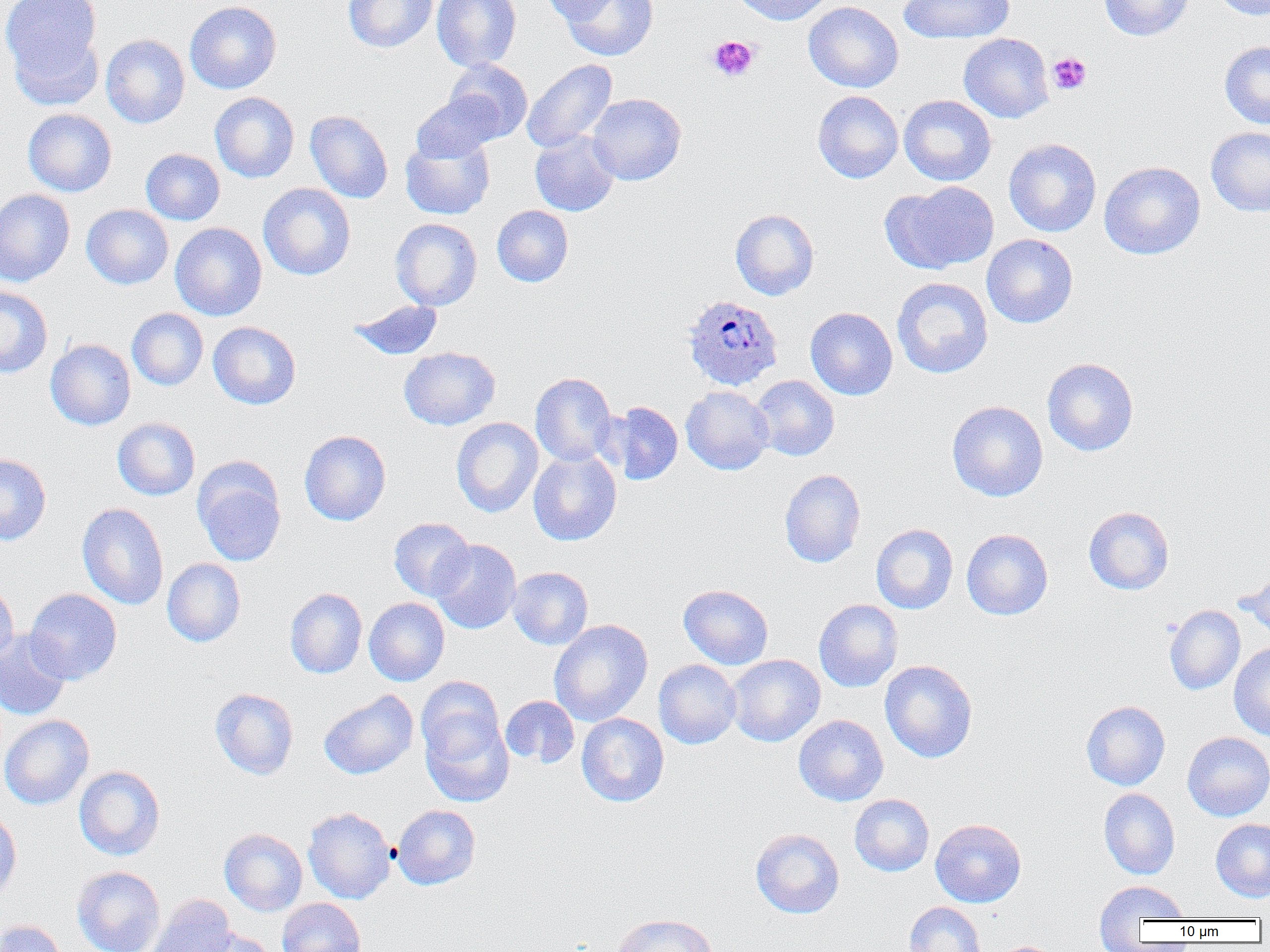
{
  "slide_level_diagnosis": "Plasmodium ovale",
  "magnification": "1000x",
  "plasmodium_ovale_infected_red_blood_cell_locations": "approximate bounding boxes as (x1,y1)-(x2,y2) corner pairs in pixels: (682,294)-(783,391)",
  "preparation": "thin blood film",
  "field_of_view": "single",
  "modality": "light microscopy",
  "image_size": "1270×952 pixels",
  "platelet_locations": "approximate bounding boxes as (x1,y1)-(x2,y2) corner pairs in pixels: (707,35)-(759,82), (1047,52)-(1092,95)",
  "uninfected_red_blood_cell_locations": "approximate bounding boxes as (x1,y1)-(x2,y2) corner pairs in pixels: (2,0)-(104,100), (343,0)-(438,53), (432,0)-(521,72), (541,0)-(621,24), (559,0)-(658,61), (731,0)-(834,26), (898,0)-(1014,44), (1098,0)-(1194,41), (1211,0)-(1269,20), (184,1)-(282,94), (803,1)-(903,93), (100,34)-(190,129), (958,34)-(1053,123), (1219,41)-(1270,130), (445,59)-(533,142), (522,59)-(617,153), (813,90)-(903,183), (210,92)-(299,183), (411,92)-(503,164), (586,93)-(686,185), (899,95)-(996,185), (22,109)-(117,197), (305,110)-(392,203), (1205,127)-(1270,217), (529,131)-(619,216), (400,133)-(496,219), (1003,138)-(1102,237), (140,148)-(225,225), (1099,161)-(1206,260), (884,180)-(999,273), (258,183)-(356,280), (0,189)-(75,286), (81,204)-(174,289), (492,205)-(573,287), (730,208)-(819,300), (390,218)-(482,310), (170,223)-(267,321), (981,234)-(1078,328), (892,277)-(993,378), (0,286)-(53,378), (348,300)-(444,360), (805,307)-(898,400), (126,308)-(208,390), (207,321)-(301,409), (45,339)-(136,430), (399,347)-(500,430), (1042,357)-(1138,456), (530,372)-(617,467), (750,375)-(839,461), (680,386)-(774,474), (947,400)-(1048,502), (601,401)-(683,486), (112,417)-(200,500), (451,417)-(543,518), (299,430)-(391,526), (528,449)-(622,546), (0,453)-(51,545), (192,458)-(286,567), (779,469)-(865,568), (77,503)-(169,610), (1083,506)-(1174,594), (388,517)-(475,601), (871,523)-(958,613), (962,528)-(1053,620), (429,538)-(522,634), (162,558)-(246,647), (508,566)-(593,649), (1238,569)-(1270,639), (0,581)-(19,667), (678,584)-(773,669), (24,588)-(122,684), (285,588)-(367,678), (364,597)-(450,686), (813,598)-(903,692), (1164,604)-(1245,695), (549,619)-(653,726), (0,629)-(72,721), (1229,642)-(1270,741), (726,654)-(825,747), (654,659)-(741,749), (879,660)-(978,763), (416,676)-(506,767), (209,688)-(299,780), (319,689)-(418,779), (500,695)-(579,768), (1081,700)-(1170,790), (420,711)-(514,808), (576,712)-(669,807), (0,715)-(94,810), (793,715)-(888,806), (1182,732)-(1270,821), (74,765)-(166,861), (1098,788)-(1180,879), (849,794)-(934,876), (392,805)-(480,889), (0,806)-(22,903), (303,807)-(396,904), (930,818)-(1026,908), (1210,819)-(1270,902), (219,828)-(307,916), (750,828)-(845,918), (72,865)-(166,952), (1094,878)-(1189,939), (147,894)-(237,952), (277,898)-(366,952), (903,901)-(986,952), (612,913)-(718,952), (0,919)-(69,952), (189,928)-(278,952), (992,941)-(1061,952)"
}